Classify this cell by malaria status.
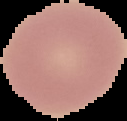
Uninfected.

Segmented cell region on a black background. Image is 127×121 pixels. From a thin blood film.